Name the parasite shown.
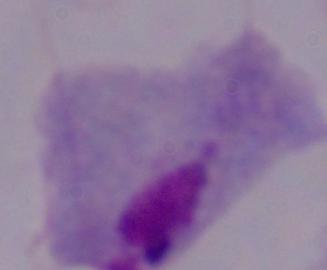
This is a trichomonad.

{
  "magnification": "1000x",
  "modality": "micrograph"
}